Locate every blood parasite and identify its species.
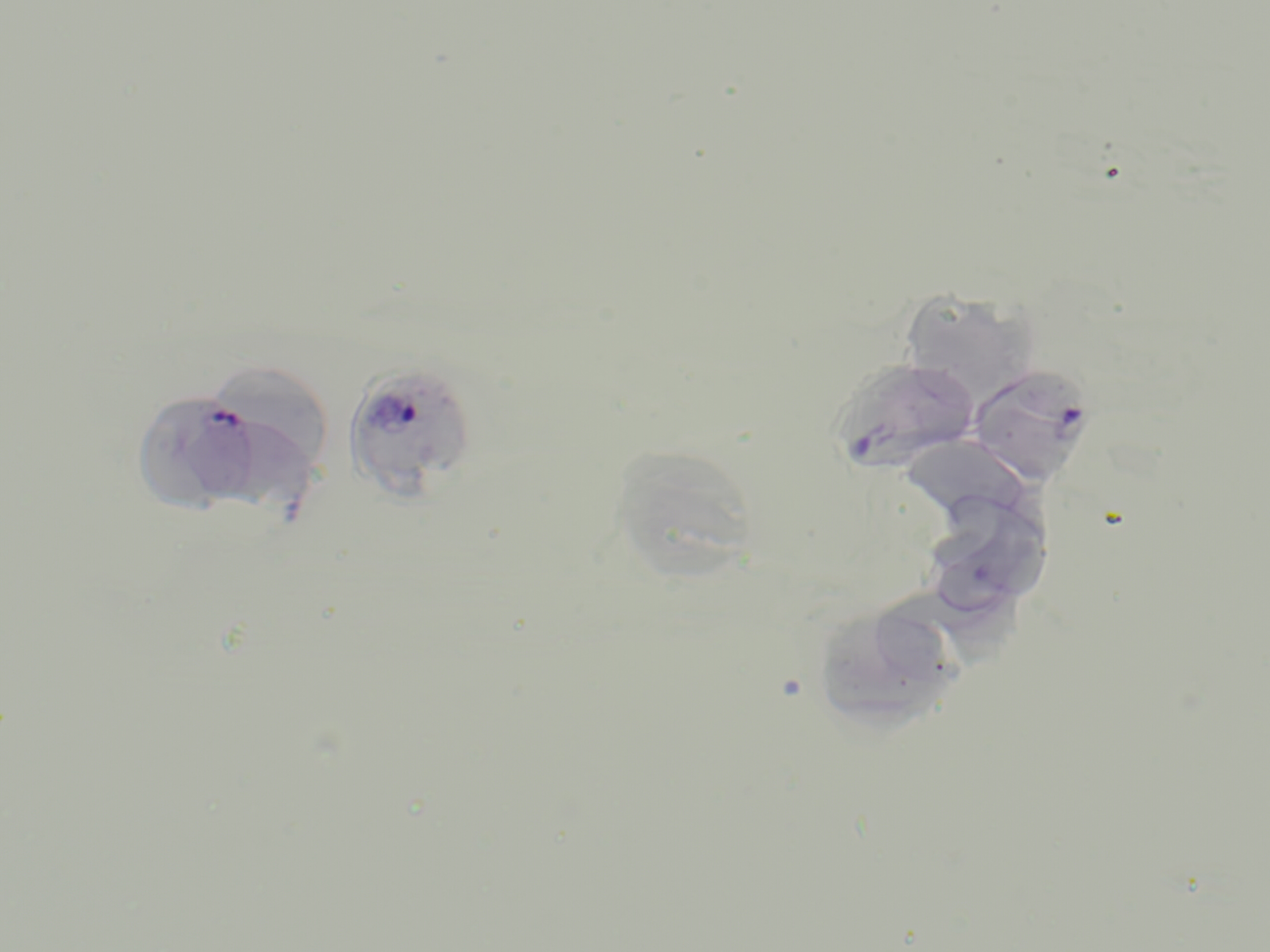

Approximate bounding boxes as [x1, y1, x2, y2] in pixels.
Plasmodium falciparum-infected red blood cells: [828, 357, 982, 475], [341, 362, 478, 502], [968, 363, 1098, 487], [132, 389, 264, 512].
No Plasmodium ovale, Plasmodium malariae, Plasmodium vivax, Babesia divergens, or Trypanosoma brucei observed.

Summary:
  - Uninfected red blood cell locations: [898, 289, 1043, 406], [201, 359, 336, 480], [902, 434, 1027, 529], [607, 452, 756, 580], [917, 488, 1055, 623], [882, 583, 1025, 682], [818, 607, 952, 733]
  - Slide-level diagnosis: Plasmodium falciparum
  - Stain: May-Grünwald-Giemsa
  - Modality: light microscopy
  - Preparation: thin blood smear
  - Image size: 1270×952 pixels
  - Field of view: one of a larger specimen
  - Magnification: 1000x